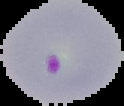

The area outside the segmented cell region is set to black. From a thin blood film. Malaria status: parasitized. Image is 124×106 pixels.